Classify this cell by malaria status.
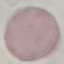

It is uninfected.

preparation = thin blood smear
capture = smartphone camera at the microscope eyepiece
stain = Giemsa
image type = automatically extracted cell patch, resized to 64 × 64 pixels